Describe the morphology of the erythrocytes.
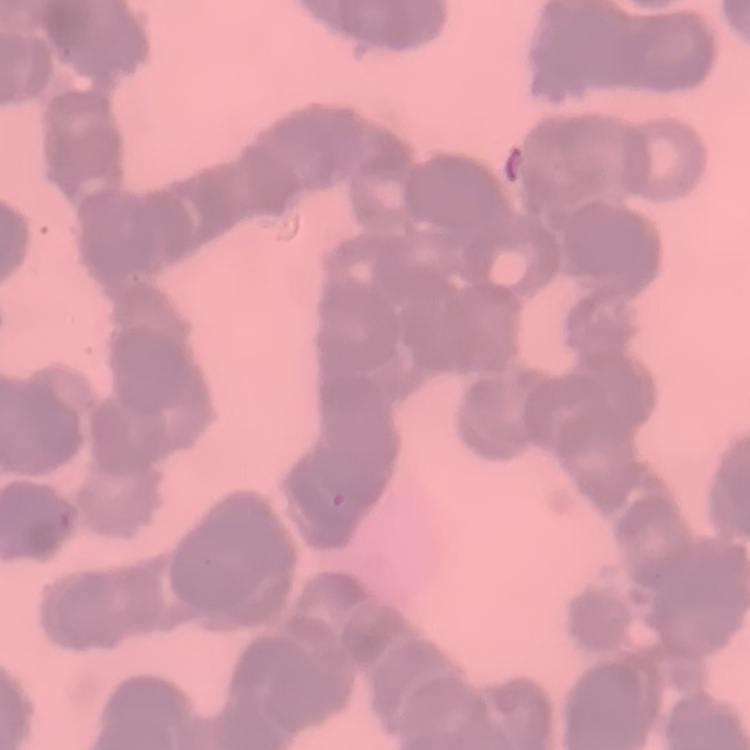
They show rouleaux formation.

Summary:
  - Stain: Field's or Giemsa
  - Image type: square crop of a larger photomicrograph
  - Preparation: thin blood film